Identify the blood parasite species.
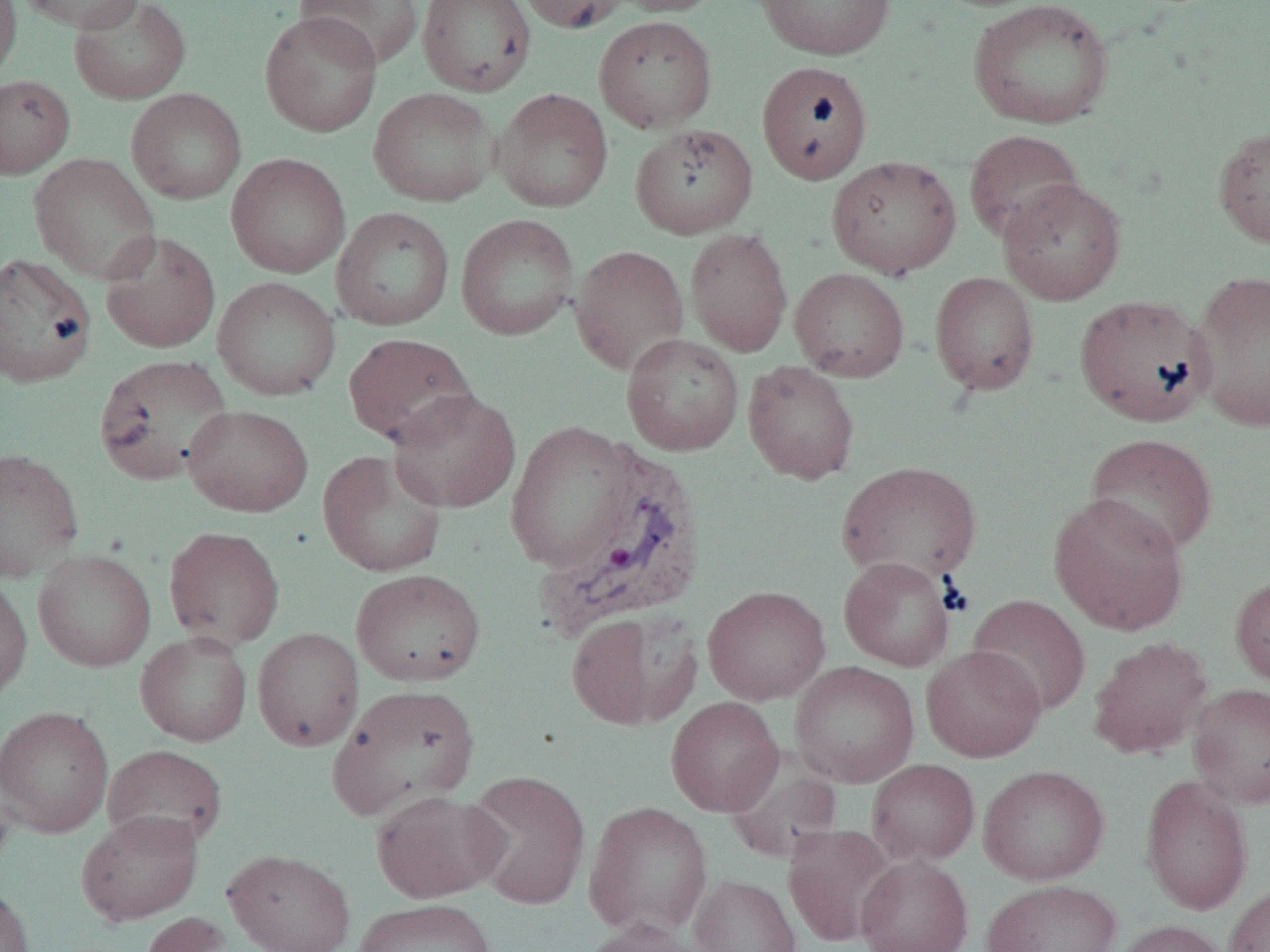
Plasmodium vivax.

modality = optical microscopy
uninfected red blood cell locations = approximate bounding boxes as [x1, y1, x2, y2] in pixels: [0, 0, 22, 82], [16, 0, 147, 33], [69, 0, 191, 105], [295, 0, 424, 68], [417, 0, 536, 96], [515, 0, 630, 34], [605, 0, 723, 16], [756, 0, 895, 60], [967, 0, 1114, 129], [259, 10, 382, 137], [593, 15, 717, 133], [756, 60, 873, 184], [0, 74, 75, 179], [368, 87, 499, 207], [126, 88, 247, 205], [493, 88, 613, 212], [629, 123, 759, 239], [1213, 126, 1270, 248], [964, 129, 1084, 245], [29, 153, 161, 284], [226, 153, 351, 278], [826, 155, 961, 279], [997, 179, 1126, 305], [331, 206, 454, 331], [456, 213, 579, 340], [685, 227, 793, 356], [100, 230, 221, 353], [570, 244, 689, 376], [0, 252, 97, 388], [789, 268, 910, 382], [1189, 268, 1270, 433], [929, 271, 1040, 395], [212, 276, 341, 401], [1073, 294, 1215, 427], [343, 332, 477, 449], [621, 332, 744, 456], [93, 354, 233, 485], [742, 360, 860, 484], [387, 388, 522, 513], [182, 404, 314, 517], [506, 421, 637, 572], [1084, 433, 1217, 558], [0, 447, 84, 582], [317, 449, 448, 577], [836, 461, 982, 585], [1048, 493, 1189, 635], [163, 525, 285, 651], [32, 549, 157, 672], [838, 556, 956, 671], [351, 569, 486, 686], [0, 572, 32, 705], [1230, 572, 1270, 692], [702, 585, 831, 705], [967, 594, 1091, 717], [566, 611, 700, 730], [252, 627, 364, 751], [135, 631, 253, 746], [1088, 636, 1212, 759], [921, 645, 1046, 762], [789, 661, 919, 787], [1188, 683, 1270, 809], [327, 684, 481, 819], [665, 696, 784, 816], [0, 704, 114, 838], [102, 744, 228, 852], [724, 755, 844, 864], [867, 759, 980, 866], [978, 765, 1110, 886], [464, 769, 591, 910], [0, 773, 17, 884], [1140, 773, 1253, 915], [370, 790, 507, 903], [582, 801, 713, 939], [75, 810, 204, 925], [782, 825, 895, 947], [224, 848, 355, 952], [855, 855, 974, 952], [689, 874, 802, 952], [981, 879, 1123, 952], [0, 883, 35, 952], [1224, 884, 1270, 952], [353, 898, 498, 952], [138, 911, 234, 952], [578, 919, 707, 952], [1112, 919, 1231, 952]
image size = 1270×952 pixels
field of view = one of a larger specimen
preparation = thin blood smear
magnification = 1000x
Plasmodium vivax-infected red blood cell locations = approximate bounding boxes as [x1, y1, x2, y2] in pixels: [533, 443, 709, 641]